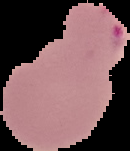
Image is 130×151 pixels. From a thin blood smear. Cell region segmented out of the field of view; the surrounding area is masked to black. Malaria status: parasitized.